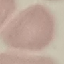

Malaria status: uninfected. Giemsa stain. Photographed with a smartphone camera at the microscope eyepiece. Thin blood film. Cell patch, automatically extracted from a larger field of view and resized to 64 × 64 pixels.